Point out every Plasmodium parasite.
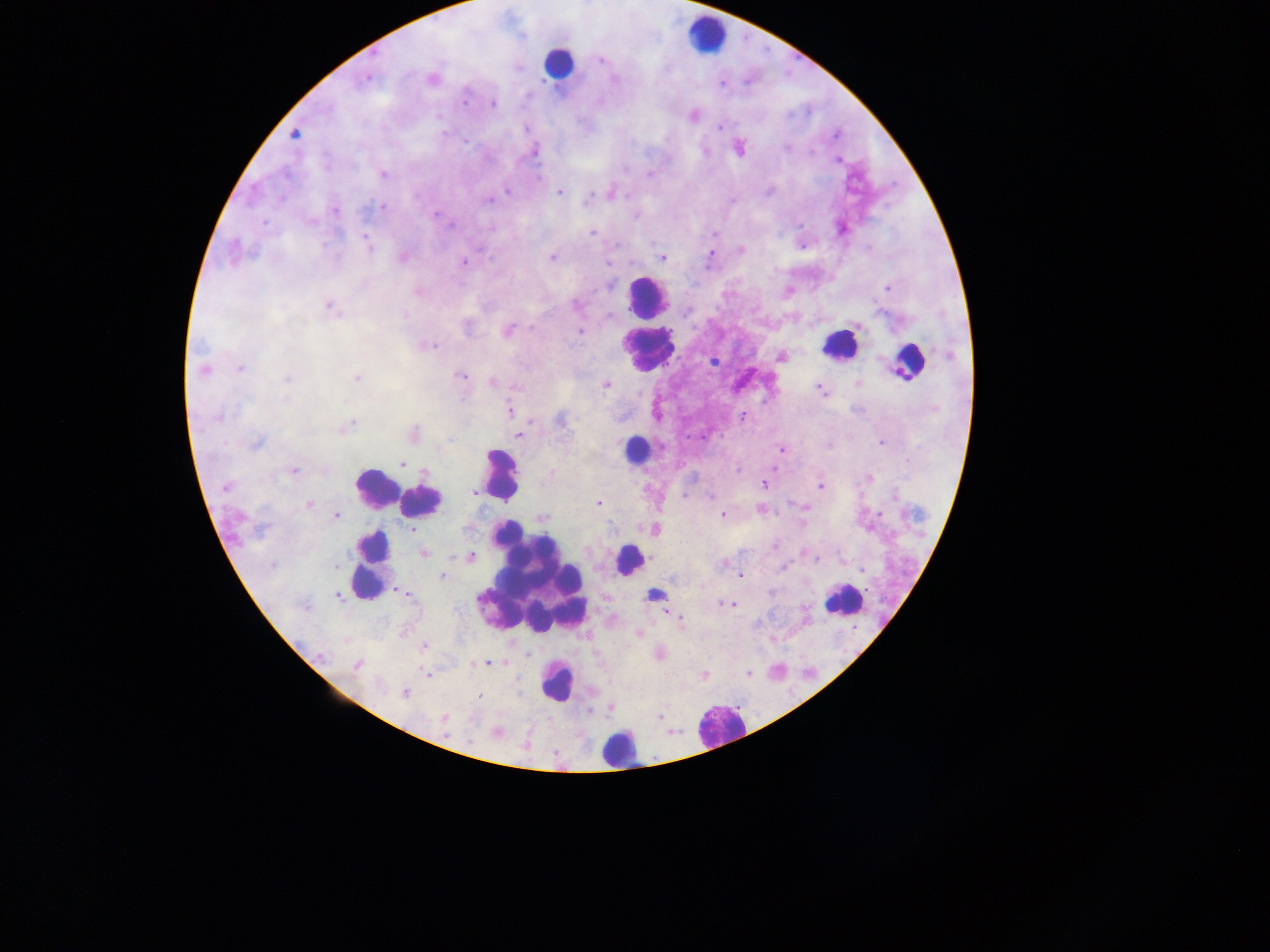

Approximate centers as x y in pixels.
Plasmodium parasites: 600 59; 366 76; 431 79; 723 83; 493 104; 693 114; 719 126; 294 134; 836 134; 738 147; 533 152; 838 160; 382 173; 560 191; 610 193; 380 207; 333 209; 636 216; 841 227; 591 232; 715 233; 366 242; 740 249; 233 252; 712 253; 552 256; 402 257; 662 257; 463 262; 608 264; 887 287; 418 290; 328 306; 606 314; 507 330; 580 330; 427 344; 949 355; 781 356; 713 360; 240 368; 203 369; 460 375; 286 378; 356 378; 493 382; 859 383; 605 384; 822 389; 510 410; 743 416; 217 417; 561 419; 344 427; 413 433; 519 434; 255 442; 881 442; 782 449; 402 463; 291 470; 738 470; 868 479; 764 484; 225 485; 821 487; 473 492; 685 496; 711 496; 597 503; 308 505; 802 506; 760 509; 878 512; 723 514; 334 515; 540 517; 653 529; 412 530; 423 553; 804 553; 470 556; 815 558; 843 559; 724 563; 783 566; 863 570; 741 575; 440 576; 395 590; 337 594; 723 603; 733 605; 671 613; 677 617; 639 634; 773 639; 424 647; 487 663; 356 665; 428 674; 703 675; 405 693; 479 696; 610 707; 661 716; 444 719; 496 732.

country = Ghana
leukocyte locations = approximate centers as x y in pixels: 707 34; 559 62; 647 297; 840 344; 648 351; 909 361; 635 450; 500 474; 375 488; 420 501; 628 559; 371 566; 534 583; 654 594; 843 599; 557 682; 719 725; 619 748
field of view = single
image size = 1270×952 pixels
preparation = thick blood smear
capture = mobile-phone photograph through a microscope